Name the cell type shown.
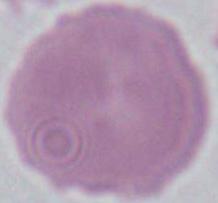
An erythrocyte.

Micrograph. 1000x magnification.